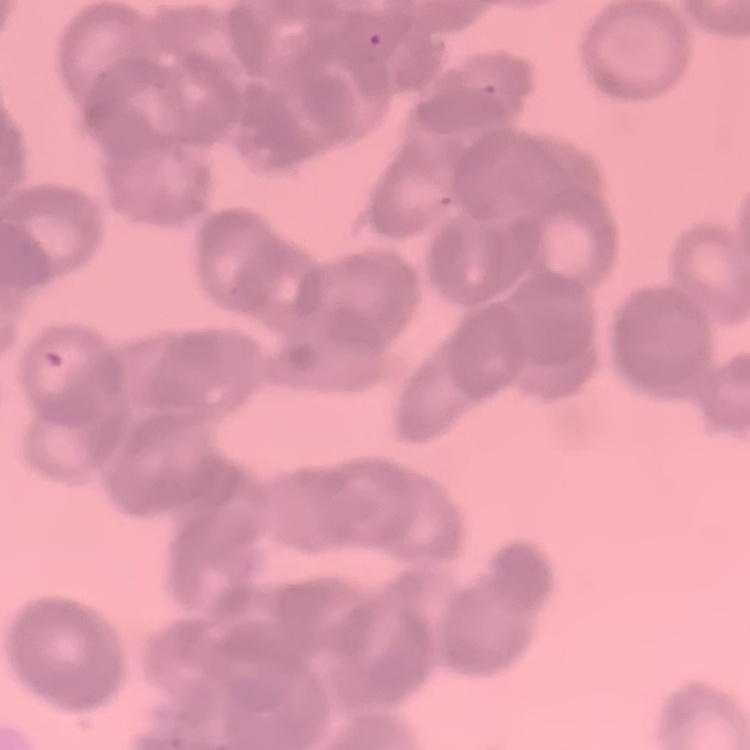
erythrocyte morphology = rouleaux formation
image type = square crop of a larger photomicrograph
stain = Field's or Giemsa
preparation = thin blood film